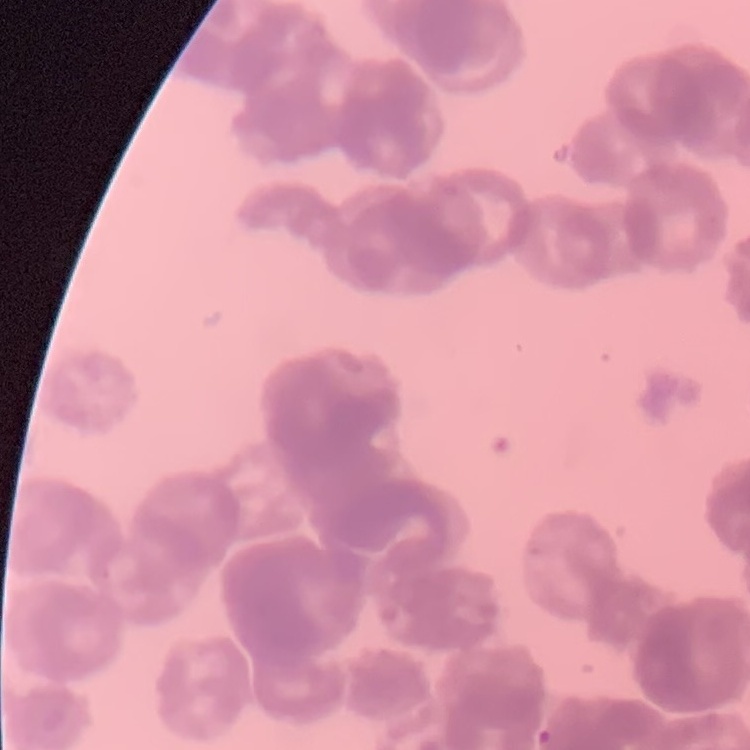

Summary:
  - Erythrocyte morphology: rouleaux formation
  - Image type: one tile cut from a larger photomicrograph
  - Preparation: thin blood smear
  - Stain: Field's or Giemsa